Classify this cell by malaria status.
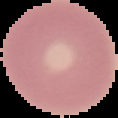
It is uninfected.

{
  "image_size": "118×118 pixels",
  "preparation": "thin blood smear",
  "image_type": "cell region segmented out of the field of view; surrounding area masked to black"
}